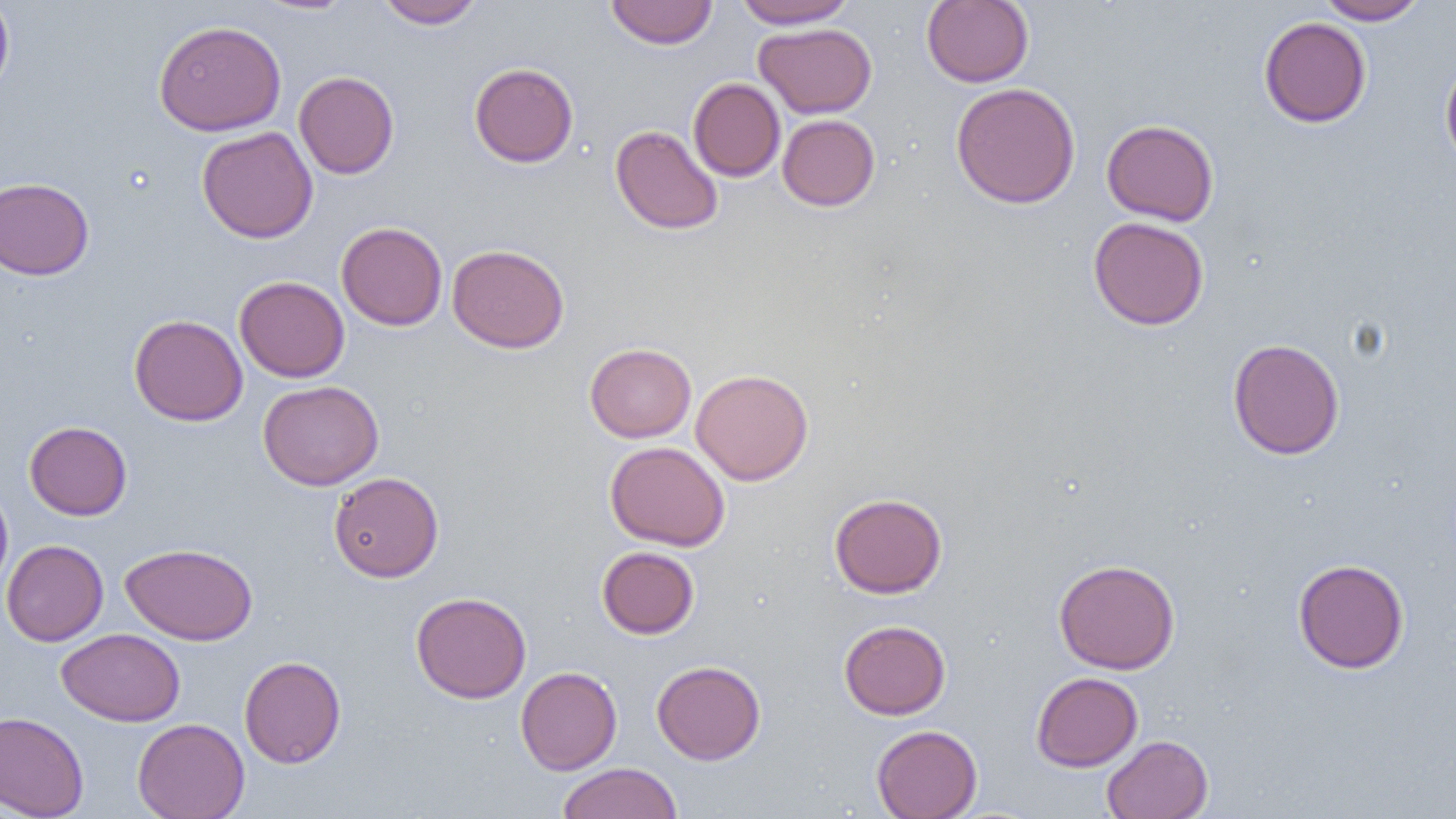

Approximate bounding boxes as named x1/y1/x2/y2 corners in pixels. Uninfected red blood cell locations: (x1=0, y1=0, x2=14, y2=99), (x1=254, y1=0, x2=357, y2=15), (x1=377, y1=0, x2=485, y2=29), (x1=605, y1=0, x2=718, y2=49), (x1=733, y1=0, x2=858, y2=29), (x1=922, y1=0, x2=1034, y2=87), (x1=1315, y1=0, x2=1428, y2=25), (x1=1259, y1=17, x2=1371, y2=128), (x1=154, y1=19, x2=286, y2=136), (x1=754, y1=23, x2=876, y2=118), (x1=1440, y1=56, x2=1456, y2=173), (x1=469, y1=62, x2=578, y2=167), (x1=293, y1=71, x2=399, y2=179), (x1=688, y1=77, x2=785, y2=182), (x1=951, y1=82, x2=1081, y2=209), (x1=778, y1=114, x2=880, y2=211), (x1=1101, y1=119, x2=1219, y2=225), (x1=610, y1=124, x2=724, y2=235), (x1=196, y1=126, x2=318, y2=243), (x1=0, y1=177, x2=94, y2=280), (x1=1088, y1=216, x2=1210, y2=330), (x1=336, y1=221, x2=448, y2=331), (x1=447, y1=244, x2=569, y2=353), (x1=234, y1=276, x2=350, y2=382), (x1=129, y1=314, x2=248, y2=426), (x1=1227, y1=337, x2=1344, y2=460), (x1=584, y1=342, x2=696, y2=443), (x1=690, y1=369, x2=814, y2=485), (x1=258, y1=380, x2=384, y2=491), (x1=24, y1=421, x2=132, y2=520), (x1=605, y1=441, x2=731, y2=551), (x1=329, y1=471, x2=444, y2=582), (x1=0, y1=481, x2=13, y2=599), (x1=829, y1=492, x2=947, y2=598), (x1=1, y1=539, x2=108, y2=646), (x1=120, y1=542, x2=258, y2=645), (x1=596, y1=546, x2=700, y2=639), (x1=1053, y1=558, x2=1180, y2=674), (x1=1292, y1=558, x2=1409, y2=673), (x1=411, y1=591, x2=531, y2=703), (x1=839, y1=619, x2=951, y2=719), (x1=57, y1=628, x2=186, y2=726), (x1=239, y1=655, x2=346, y2=768), (x1=652, y1=659, x2=766, y2=765), (x1=516, y1=666, x2=622, y2=775), (x1=1031, y1=671, x2=1143, y2=772), (x1=0, y1=711, x2=89, y2=819), (x1=133, y1=718, x2=250, y2=819), (x1=871, y1=724, x2=982, y2=818), (x1=1101, y1=734, x2=1213, y2=819), (x1=557, y1=762, x2=683, y2=819). Slide-level diagnosis: no evidence of blood parasites. Thin blood film. Image is 1456×819 pixels. 1000x magnification. Single field of view. Optical microscopy.